Classify this cell by malaria status.
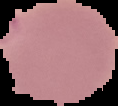

Parasitized.

Summary:
  - Preparation: thin blood smear
  - Image type: cell region segmented out of the field of view; surrounding area masked to black
  - Image size: 118×106 pixels